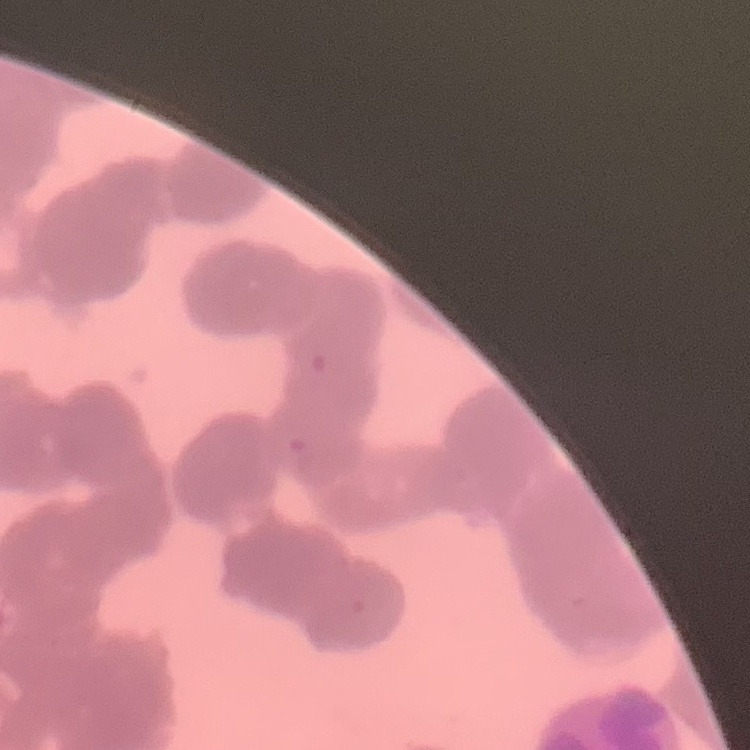
The red blood cells exhibit rouleaux formation. Square crop of a larger photomicrograph. Thin blood smear. Stained with either Field's or Giemsa.